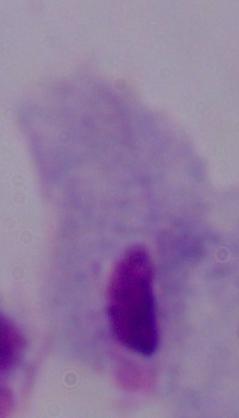

{
  "identification": "trichomonad",
  "magnification": "1000x",
  "modality": "photomicrograph"
}